Identify the parasite.
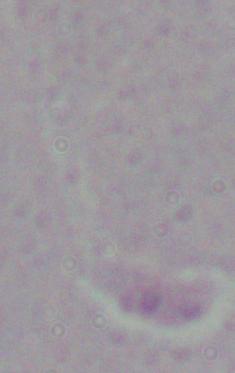
Leishmania.

Summary:
  - Magnification: 1000x
  - Modality: micrograph